Identify the cell.
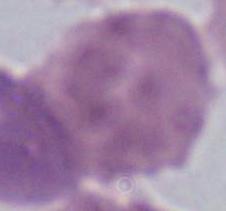
An erythrocyte.

Summary:
  - Modality: photomicrograph
  - Magnification: 1000x